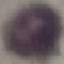
Summary:
  - Malaria status: uninfected
  - Capture: smartphone through the microscope eyepiece
  - Stain: Giemsa
  - Image type: cell patch, automatically extracted from a larger field of view and resized to 64 × 64 pixels
  - Preparation: thin smear